Classify this cell by malaria status.
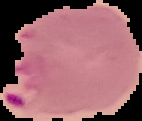
Parasitized.

Image is 142×121 pixels. From a thin blood film. Segmented cell region on a black background.